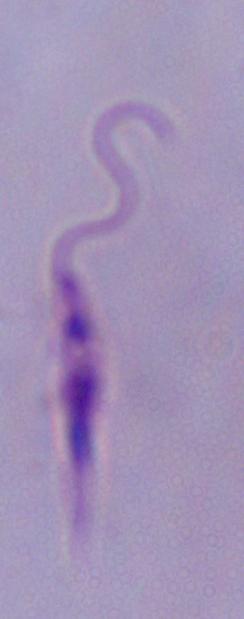

Summary:
  - Modality: micrograph
  - Magnification: 1000x
  - Identification: Leishmania